Point out each malaria parasite.
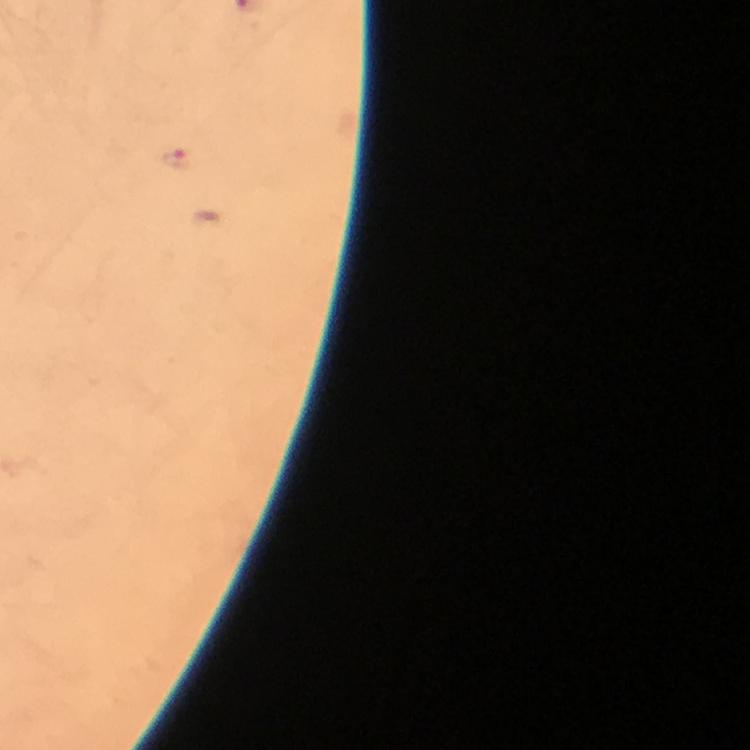

Approximate centers as [x, y] in pixels.
Malaria parasites: [176, 158].

context = from a diagnostic examination for malaria
magnification = 100x
preparation = thick blood smear
image size = 750×750 pixels
stain = Giemsa
capture = smartphone photograph through a microscope
immersion oil = applied
cropped from = a single field of view